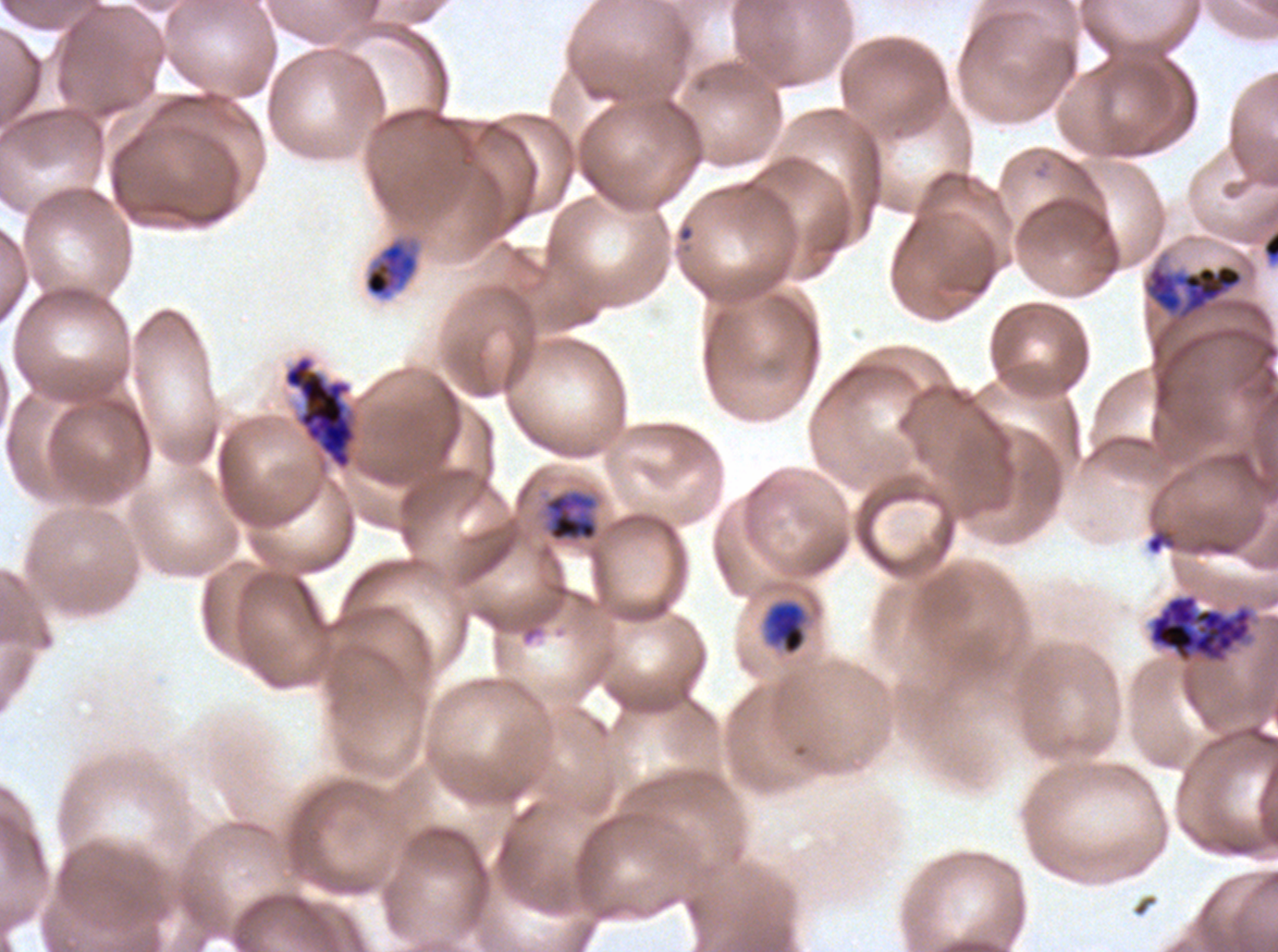

Approximate bounding boxes as (x1, y1, x2, y2) in pixels. Late schizont locations: (1149, 595, 1251, 660). Object labeled both ring and mid trophozoite by the source: (542, 488, 599, 543). Early schizont locations: (1144, 263, 1244, 322), (283, 356, 356, 470). Debris locations: (1146, 530, 1175, 555). Mid trophozoite locations: (363, 237, 421, 300), (765, 601, 806, 655). P. falciparum cultured ex vivo for 24 to 48 hours, from a patient in The Gambia. Image is 1278×952 pixels. Giemsa-stained preparation. One sub-image of a larger composite. Life-cycle stages observed: mid trophozoite, early schizont, late schizont. Thin blood smear.